Evaluate for malaria.
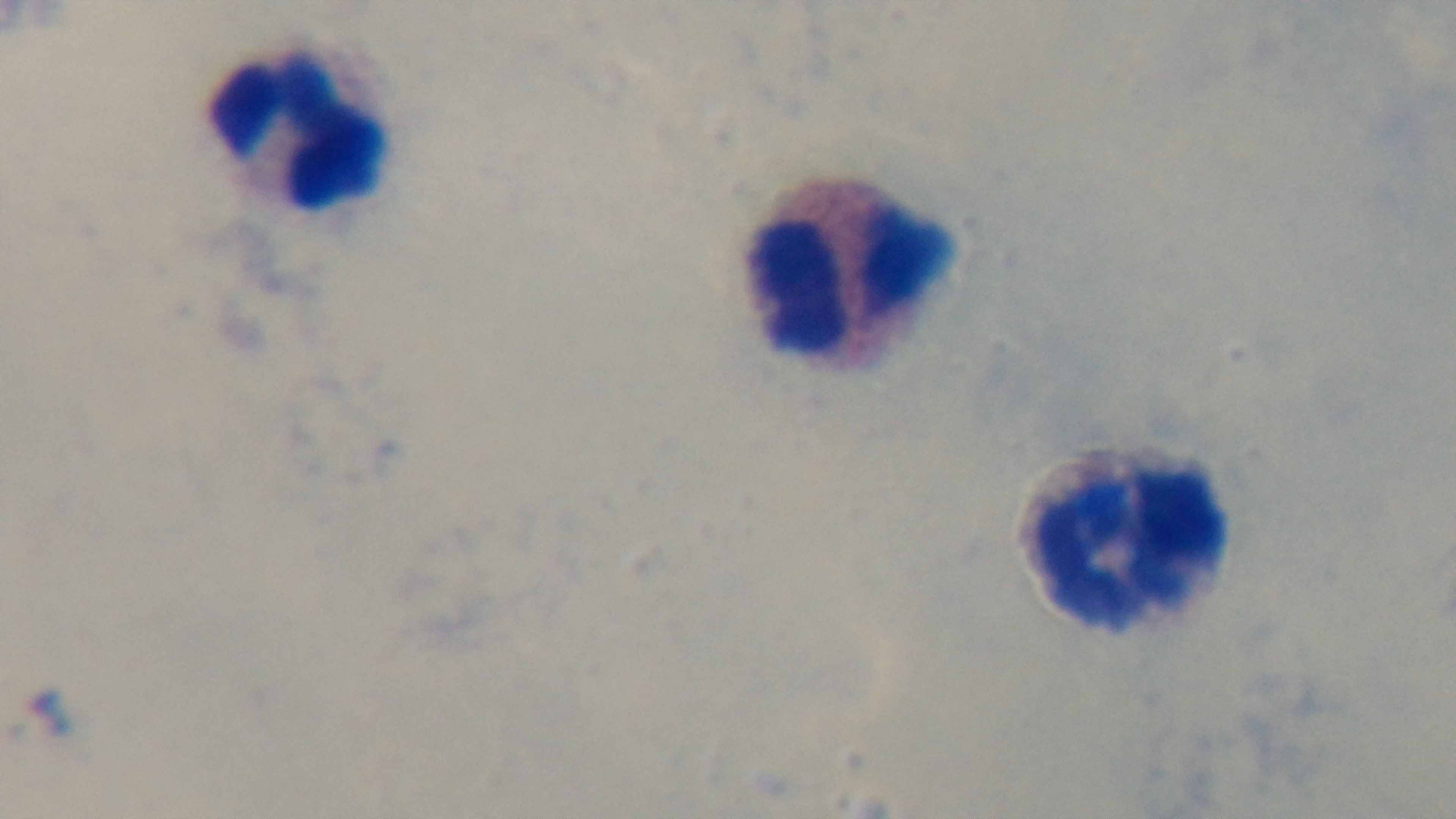

It is uninfected.

Light microscopy. One field from the slide. Mounted 4K digital camera. Preparation: thick smear. 100x oil-immersion objective. Giemsa stain.